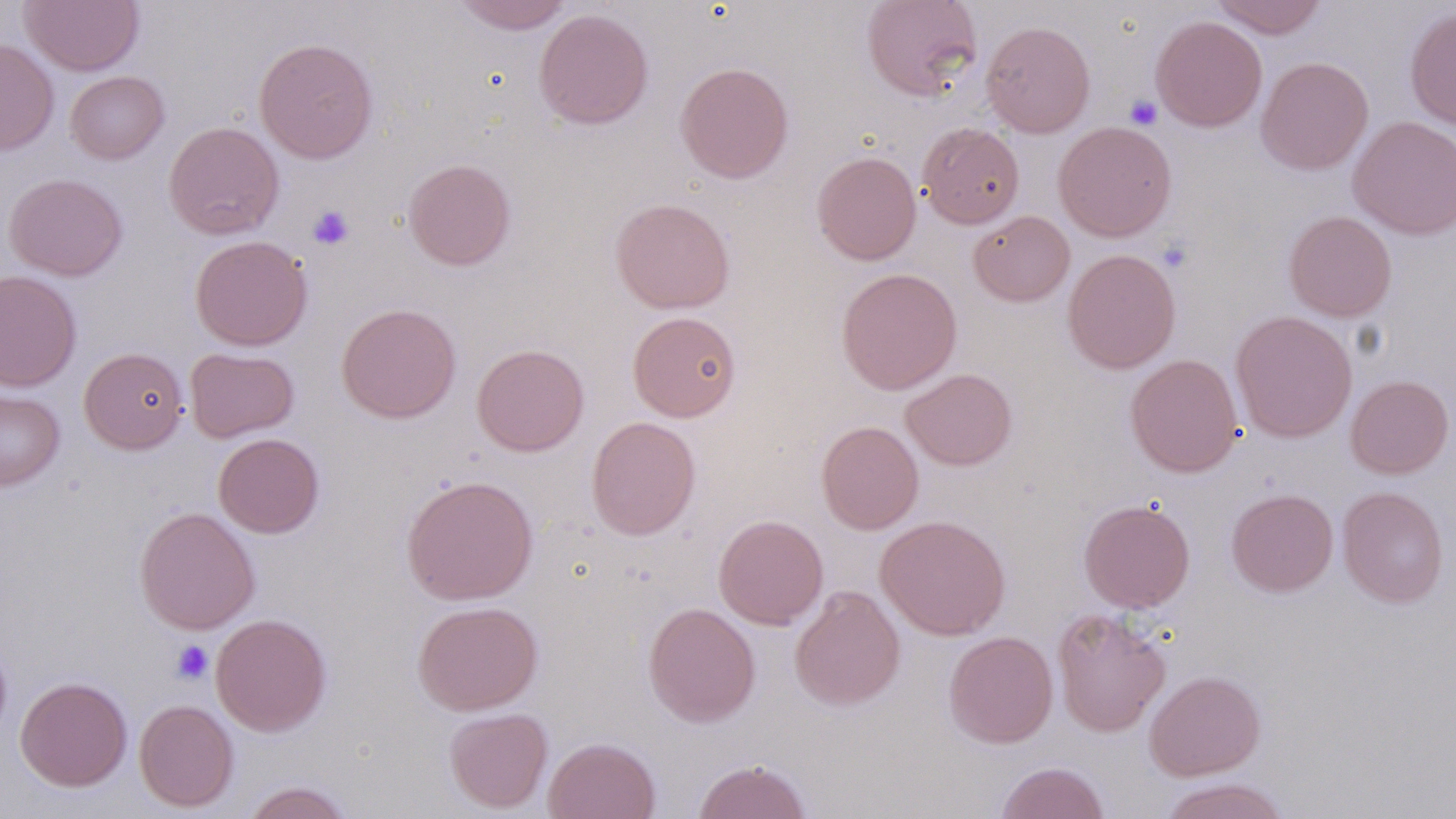
Summary:
  - Coordinate format: approximate bounding boxes as named x1/y1/x2/y2 corners in pixels
  - Uninfected red blood cell locations: (x1=20, y1=0, x2=144, y2=75), (x1=451, y1=0, x2=575, y2=34), (x1=860, y1=0, x2=983, y2=102), (x1=1209, y1=0, x2=1328, y2=39), (x1=1404, y1=6, x2=1456, y2=130), (x1=534, y1=9, x2=653, y2=130), (x1=1151, y1=15, x2=1267, y2=132), (x1=981, y1=20, x2=1096, y2=137), (x1=254, y1=37, x2=379, y2=164), (x1=0, y1=40, x2=59, y2=156), (x1=1256, y1=56, x2=1373, y2=175), (x1=674, y1=61, x2=794, y2=183), (x1=65, y1=70, x2=169, y2=164), (x1=1347, y1=115, x2=1456, y2=239), (x1=163, y1=121, x2=284, y2=240), (x1=1052, y1=121, x2=1177, y2=241), (x1=917, y1=122, x2=1025, y2=229), (x1=812, y1=151, x2=921, y2=265), (x1=403, y1=158, x2=516, y2=270), (x1=4, y1=173, x2=128, y2=281), (x1=610, y1=197, x2=735, y2=314), (x1=1283, y1=210, x2=1397, y2=322), (x1=968, y1=211, x2=1075, y2=307), (x1=189, y1=235, x2=312, y2=351), (x1=1063, y1=249, x2=1181, y2=373), (x1=836, y1=267, x2=962, y2=395), (x1=0, y1=269, x2=82, y2=392), (x1=336, y1=303, x2=461, y2=423), (x1=627, y1=310, x2=741, y2=422), (x1=1230, y1=310, x2=1357, y2=443), (x1=472, y1=343, x2=589, y2=456), (x1=79, y1=347, x2=188, y2=454), (x1=185, y1=347, x2=299, y2=443), (x1=1124, y1=353, x2=1243, y2=477), (x1=901, y1=368, x2=1017, y2=470), (x1=1345, y1=374, x2=1454, y2=478), (x1=0, y1=387, x2=65, y2=491), (x1=586, y1=415, x2=701, y2=540), (x1=816, y1=421, x2=924, y2=534), (x1=213, y1=433, x2=324, y2=538), (x1=401, y1=475, x2=539, y2=605), (x1=1337, y1=486, x2=1449, y2=608), (x1=1226, y1=488, x2=1338, y2=597), (x1=1079, y1=498, x2=1195, y2=612), (x1=134, y1=506, x2=260, y2=634), (x1=714, y1=514, x2=829, y2=629), (x1=876, y1=515, x2=1011, y2=640), (x1=789, y1=585, x2=905, y2=711), (x1=412, y1=600, x2=543, y2=715), (x1=642, y1=602, x2=761, y2=727), (x1=1052, y1=607, x2=1171, y2=738), (x1=210, y1=613, x2=331, y2=736), (x1=943, y1=630, x2=1058, y2=748), (x1=0, y1=637, x2=13, y2=745), (x1=1144, y1=670, x2=1265, y2=780), (x1=15, y1=676, x2=133, y2=792), (x1=134, y1=699, x2=239, y2=811), (x1=444, y1=707, x2=553, y2=813), (x1=544, y1=736, x2=661, y2=819), (x1=693, y1=758, x2=812, y2=819), (x1=995, y1=761, x2=1109, y2=819), (x1=1156, y1=777, x2=1292, y2=819), (x1=240, y1=781, x2=356, y2=819)
  - Platelet locations: (x1=1124, y1=94, x2=1163, y2=130), (x1=308, y1=205, x2=354, y2=250), (x1=1156, y1=239, x2=1194, y2=274), (x1=171, y1=640, x2=214, y2=684)
  - Slide-level diagnosis: negative for blood parasites
  - Image size: 1456×819 pixels
  - Preparation: thin blood film
  - Stain: May-Grünwald-Giemsa
  - Modality: optical microscopy
  - Magnification: 1000x
  - Field of view: single